State which parasite is depicted.
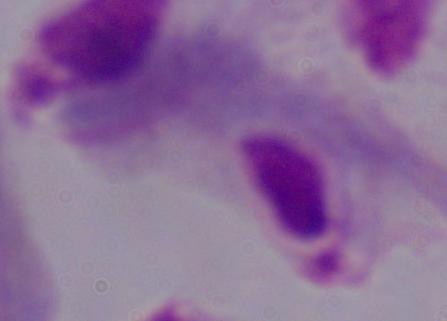
A trichomonad.

Photomicrograph. 1000x magnification.